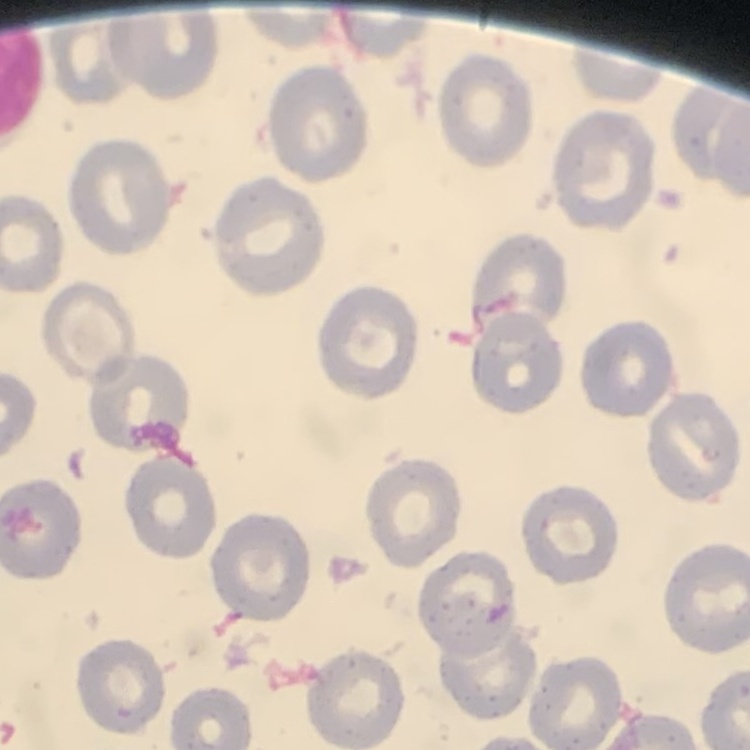
erythrocyte_morphology: no rouleaux formation
image_type: square crop of a larger photomicrograph
preparation: thin peripheral smear
stain: Field's or Giemsa